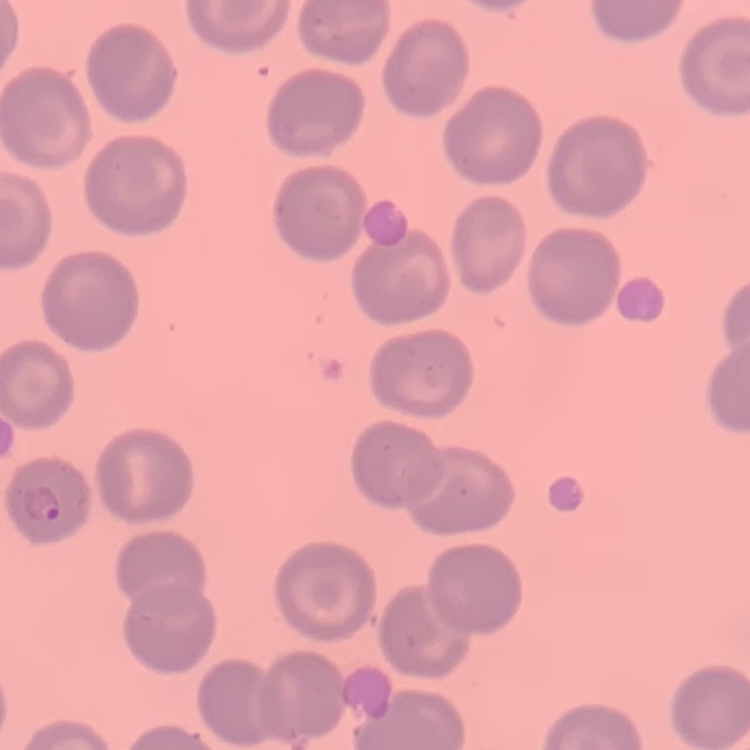

Summary:
  - Red blood cell morphology: no rouleaux formation
  - Stain: Field's or Giemsa
  - Preparation: thin blood smear
  - Image type: square crop of a larger photomicrograph